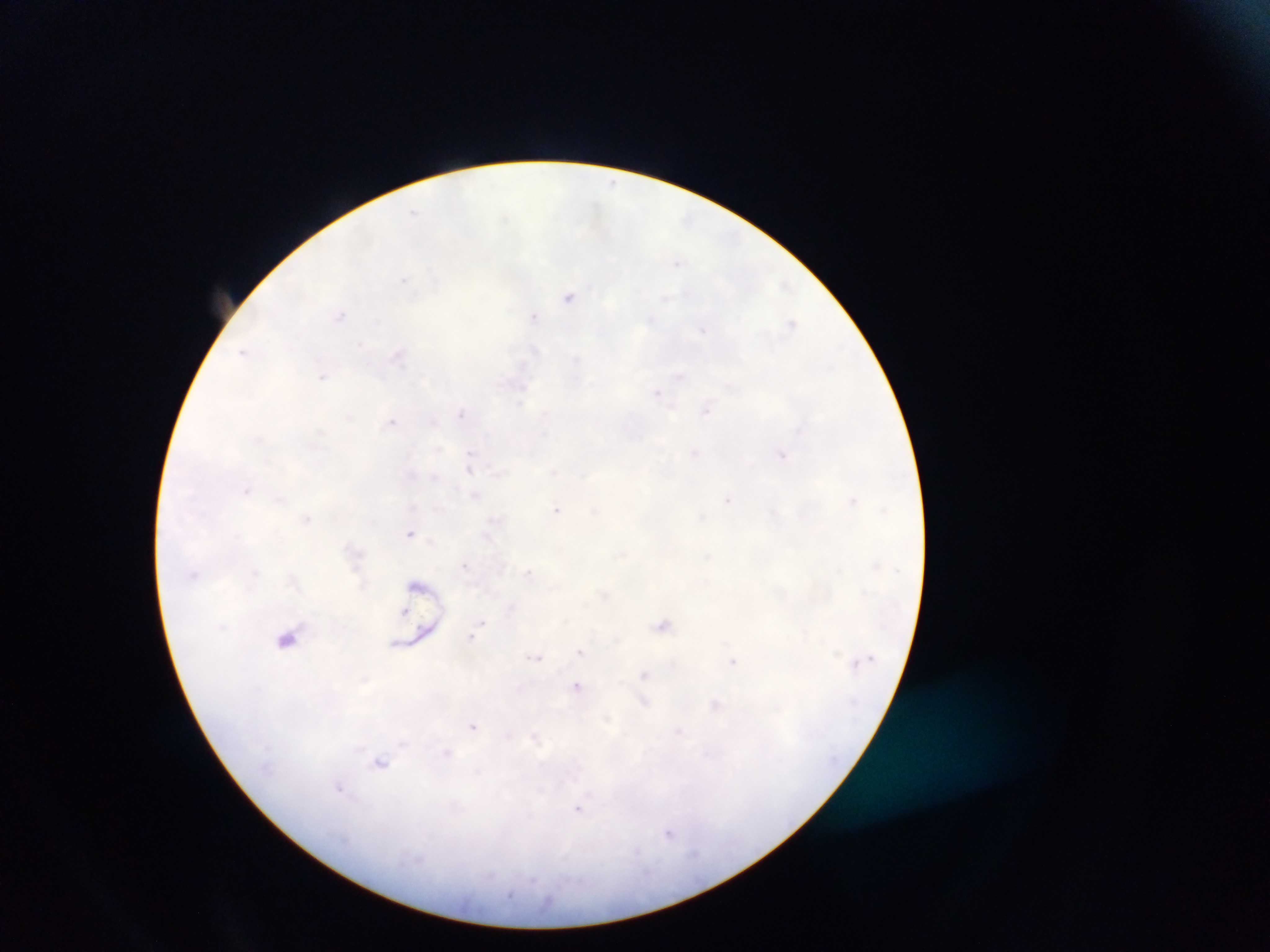 Approximate centers as (x, y) in pixels. Malaria parasite locations: (679, 261), (569, 296), (340, 316), (534, 317), (792, 324), (243, 351), (399, 355), (323, 375), (658, 392), (706, 410), (463, 413), (393, 421), (697, 453), (782, 455), (471, 456), (474, 495), (729, 500), (853, 501), (558, 509), (307, 518), (411, 533), (466, 565), (529, 573), (512, 607), (405, 610), (482, 622), (664, 625), (472, 637), (287, 638), (581, 651), (535, 656), (734, 662), (646, 675), (578, 687), (644, 703), (717, 704), (473, 726), (679, 732), (536, 738), (380, 761), (339, 788), (579, 808), (670, 833). Thick blood smear. Photographed through a microscope with a mobile-phone camera. One field of view. Image is 1270×952 pixels. Sample from Ghana.